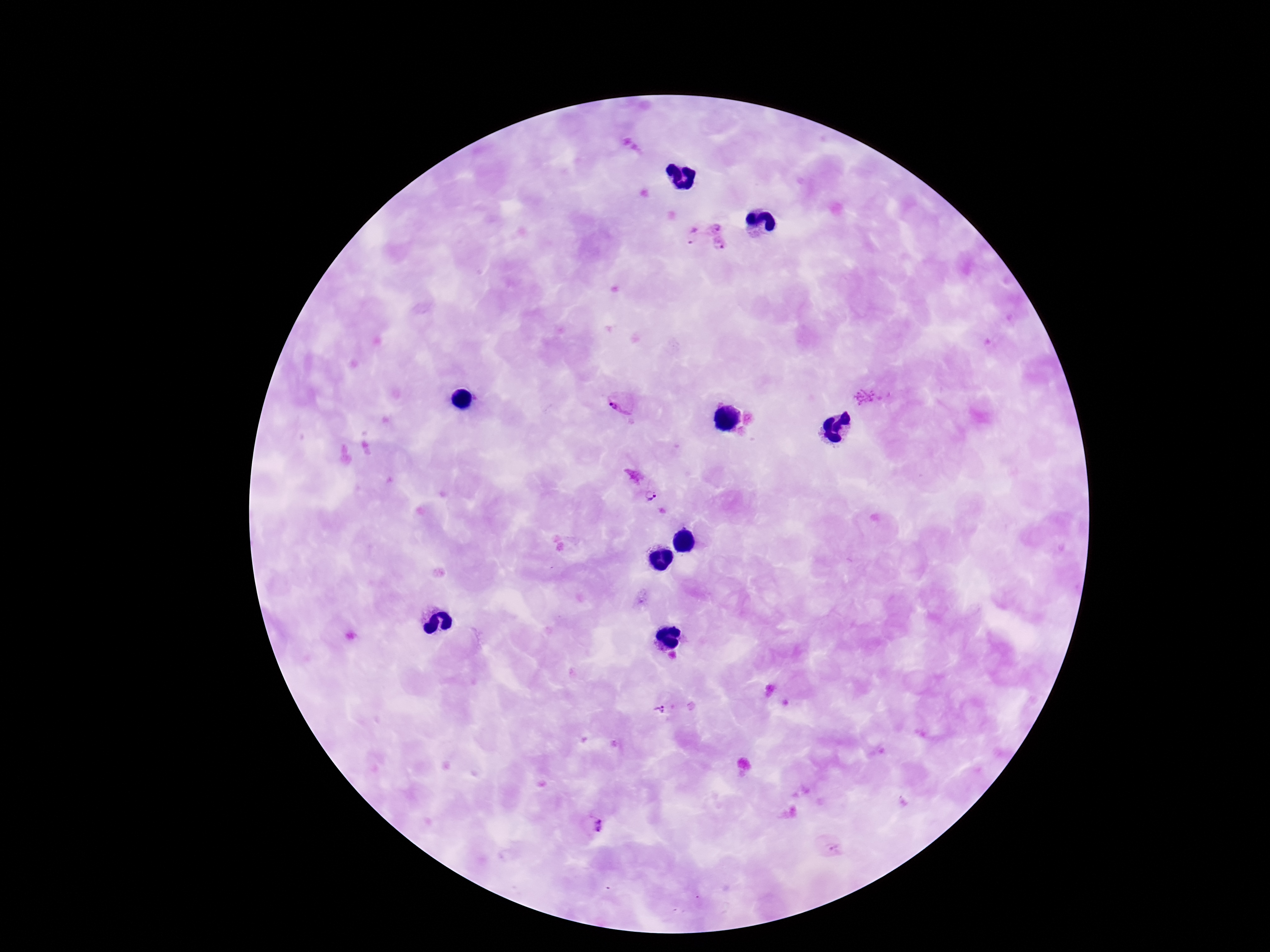
Approximate centers as {x, y} in pixels.
Summary:
  - Plasmodium parasite locations: {715, 227}, {693, 235}, {722, 247}, {865, 398}, {621, 400}, {634, 475}, {650, 495}, {660, 712}, {598, 826}, {837, 847}
  - Patient malaria status: infected
  - Image size: 1270×952 pixels
  - Field of view: single
  - Capture: smartphone camera through the microscope eyepiece
  - Preparation: thick blood smear
  - Stain: Giemsa
  - Magnification: 100x